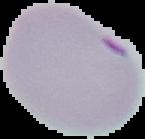
{
  "preparation": "thin blood smear",
  "result": "malaria parasites identified",
  "image_size": "145×139 pixels",
  "image_type": "cell region segmented out of the field of view; surrounding area masked to black"
}